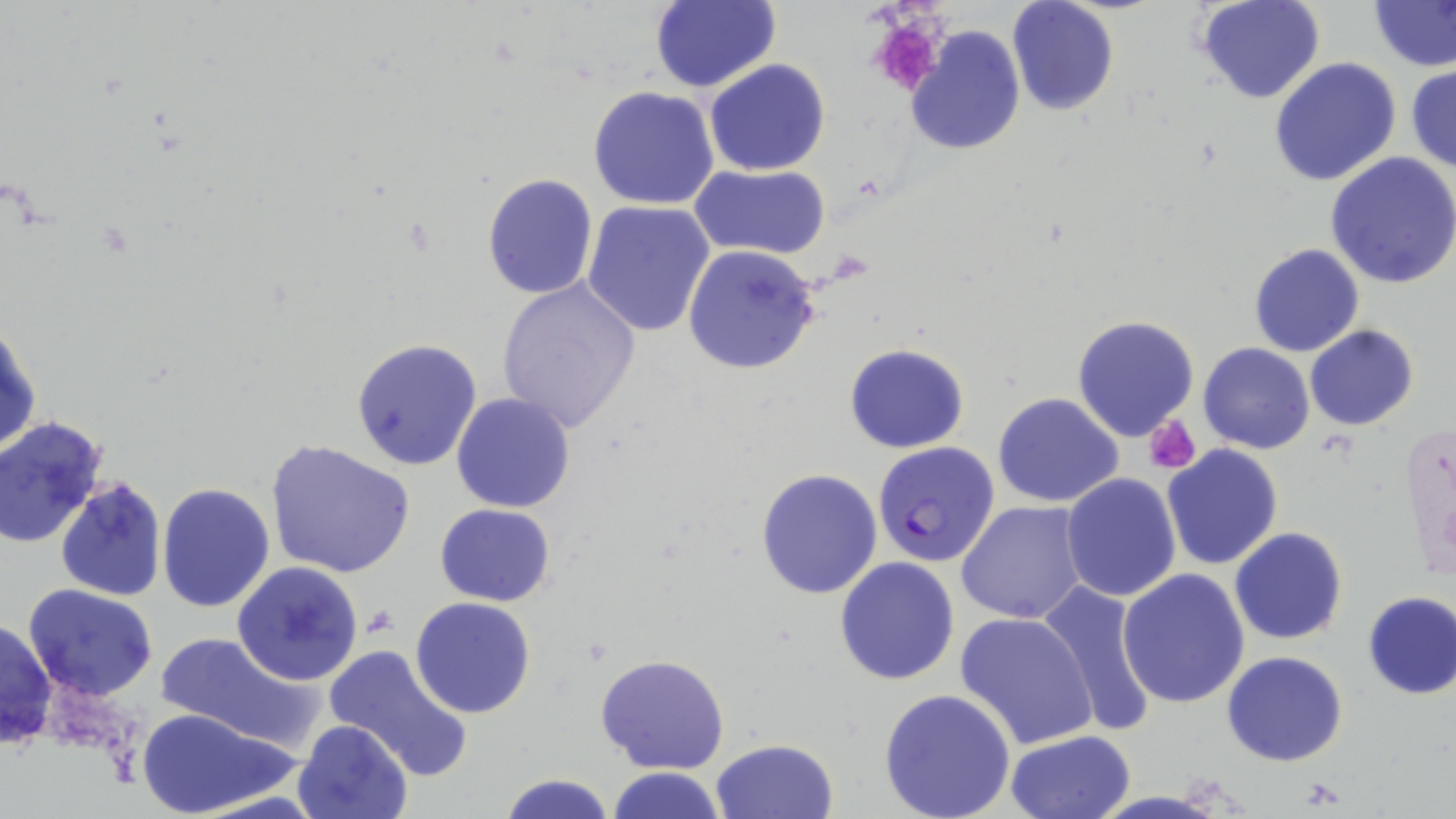
slide-level diagnosis = Plasmodium falciparum
platelet locations = approximate bounding boxes as (x1,y1)-(x2,y2) corner pairs in pixels: (865,13)-(949,97), (1143,415)-(1201,472), (363,606)-(396,637)
stain = May-Grünwald-Giemsa
uninfected red blood cell locations = approximate bounding boxes as (x1,y1)-(x2,y2) corner pairs in pixels: (649,0)-(781,93), (1006,0)-(1120,117), (1195,0)-(1326,104), (1370,3)-(1456,70), (905,24)-(1025,156), (1268,57)-(1402,188), (703,58)-(831,177), (1406,65)-(1456,176), (587,86)-(720,210), (1326,151)-(1456,288), (691,163)-(831,261), (481,174)-(598,300), (583,200)-(717,338), (1247,243)-(1365,358), (683,244)-(819,375), (496,277)-(641,433), (1071,315)-(1200,441), (1,316)-(40,461), (1305,324)-(1419,430), (352,337)-(483,470), (843,342)-(969,454), (1199,343)-(1316,454), (451,392)-(578,513), (993,392)-(1125,507), (0,416)-(108,546), (267,439)-(413,579), (1162,444)-(1285,570), (755,467)-(884,599), (1061,473)-(1182,604), (55,476)-(167,601), (156,482)-(275,614), (957,501)-(1090,625), (434,503)-(556,606), (1229,526)-(1348,644), (834,555)-(961,686), (232,561)-(364,685), (1119,567)-(1251,707), (1036,582)-(1160,738), (24,585)-(157,700), (1360,590)-(1456,701), (409,597)-(537,719), (956,611)-(1099,749), (1,617)-(57,751), (156,633)-(317,749), (323,643)-(475,781), (1221,650)-(1348,766), (596,653)-(730,773), (878,688)-(1015,819), (136,705)-(300,816), (293,718)-(413,819), (1005,729)-(1135,818), (709,738)-(839,819), (603,767)-(727,819), (500,773)-(616,819)
magnification = 1000x
modality = light microscopy
preparation = thin blood film
field of view = one of a larger specimen
Plasmodium falciparum-infected red blood cell locations = approximate bounding boxes as (x1,y1)-(x2,y2) corner pairs in pixels: (872,440)-(1001,568)
image size = 1456×819 pixels